Mark where platelets are.
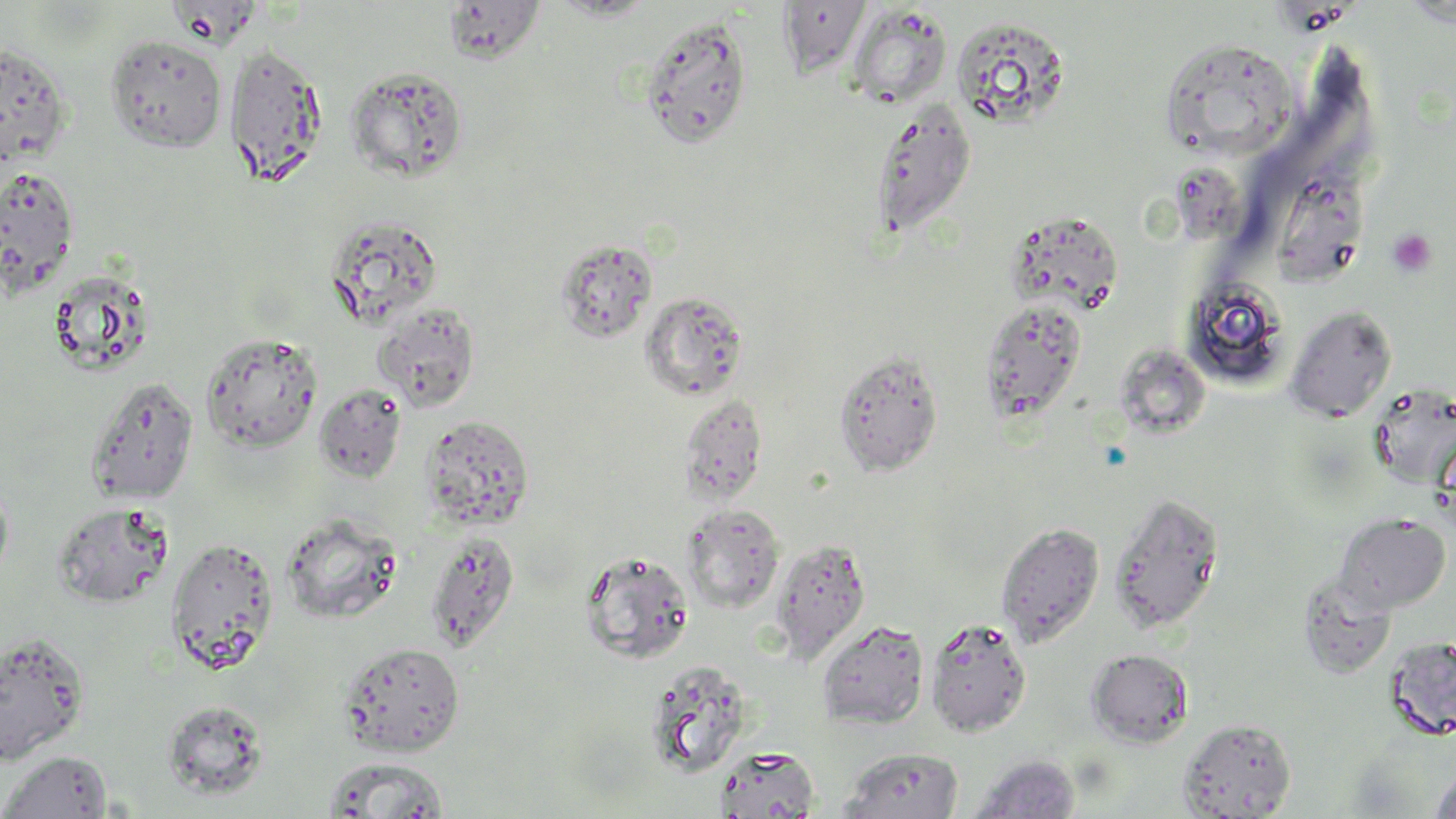
Approximate bounding boxes as (x1,y1)-(x2,y2) corner pairs in pixels.
Platelets: (1387,228)-(1437,277).

Uninfected red blood cell locations: (778,0)-(872,80), (442,2)-(545,64), (846,5)-(952,109), (639,15)-(754,149), (950,16)-(1072,129), (105,34)-(227,153), (1159,38)-(1298,160), (0,43)-(72,166), (224,43)-(327,185), (345,65)-(469,182), (870,98)-(977,238), (1,166)-(80,297), (323,215)-(443,330), (1003,216)-(1126,320), (554,238)-(658,344), (47,269)-(155,376), (1178,275)-(1290,390), (639,291)-(750,401), (979,299)-(1087,424), (373,302)-(481,412), (1285,305)-(1397,422), (200,331)-(323,453), (1125,346)-(1211,438), (833,348)-(943,476), (86,377)-(199,505), (314,384)-(407,483), (1369,384)-(1456,490), (678,395)-(768,506), (420,415)-(534,531), (0,474)-(14,590), (1108,491)-(1224,633), (53,502)-(175,608), (682,504)-(785,614), (281,512)-(402,624), (1334,513)-(1450,613), (996,521)-(1105,648), (424,531)-(520,652), (166,537)-(279,674), (770,537)-(871,665), (579,549)-(695,665), (1297,571)-(1396,680), (924,618)-(1032,738), (816,620)-(929,730), (0,631)-(90,766), (1384,635)-(1456,740), (340,642)-(465,756), (1086,648)-(1193,747), (643,660)-(754,779), (161,699)-(269,800), (1178,718)-(1296,818), (713,746)-(820,819), (840,747)-(964,819), (1,750)-(113,818), (968,754)-(1081,819), (322,756)-(450,818), (1427,766)-(1456,819). Slide-level diagnosis: negative for blood parasites. Single field of view. Optical microscopy. Thin blood smear. Image is 1456×819 pixels. May-Grünwald-Giemsa-stained preparation. Captured at 1000x magnification.